Outline each blood parasite and name the species.
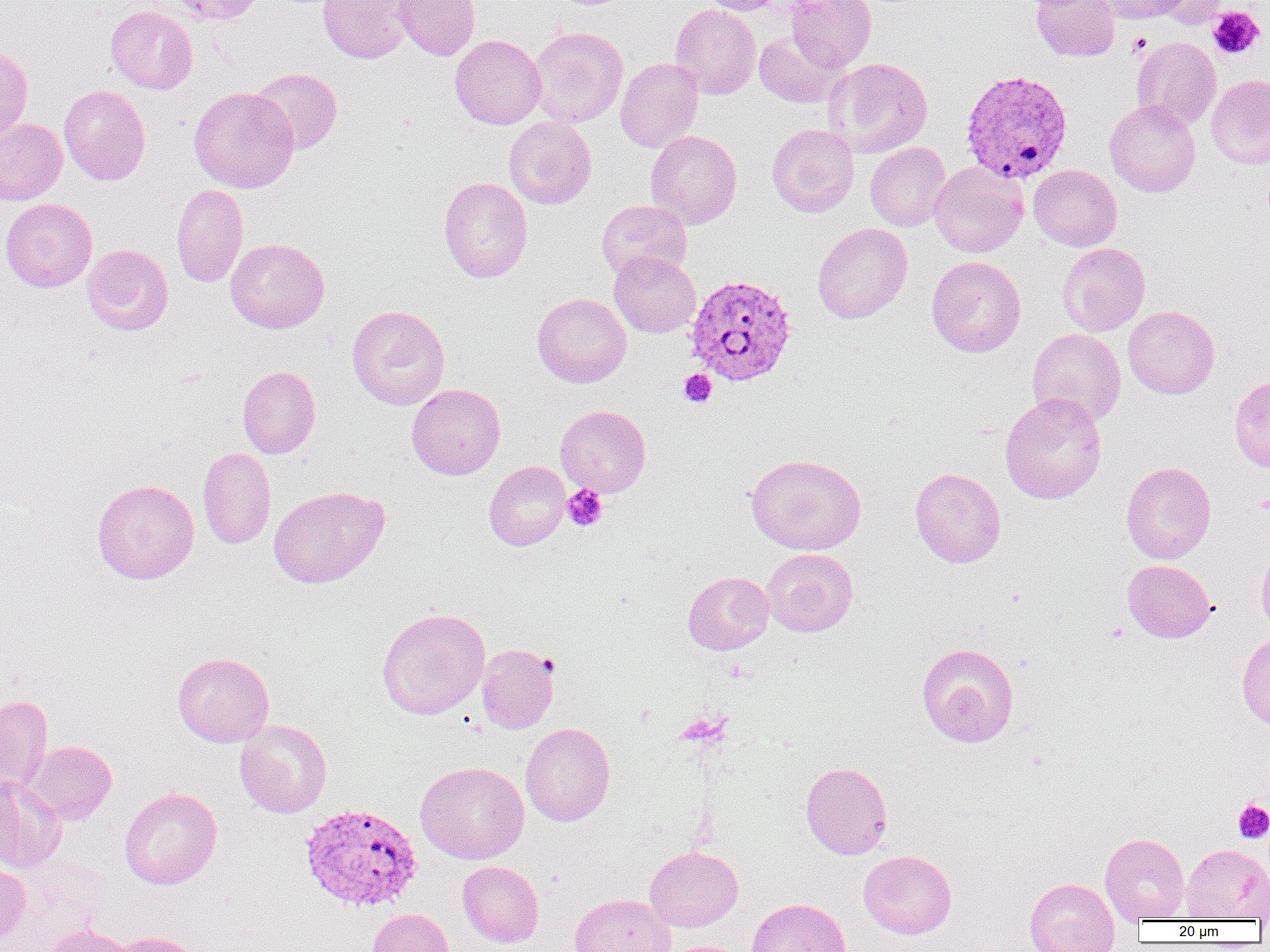

Approximate bounding boxes as named x1/y1/x2/y2 corners in pixels.
Plasmodium vivax-infected red blood cells: (x1=961, y1=69, x2=1073, y2=184), (x1=686, y1=274, x2=797, y2=386), (x1=300, y1=803, x2=423, y2=912).
No Plasmodium falciparum, Plasmodium ovale, Plasmodium malariae, Babesia divergens, or Trypanosoma brucei observed.

Uninfected red blood cell locations: (x1=164, y1=0, x2=266, y2=26), (x1=317, y1=0, x2=416, y2=63), (x1=394, y1=0, x2=480, y2=60), (x1=700, y1=0, x2=784, y2=14), (x1=786, y1=0, x2=876, y2=72), (x1=1032, y1=0, x2=1119, y2=61), (x1=1095, y1=0, x2=1190, y2=24), (x1=1154, y1=0, x2=1229, y2=29), (x1=670, y1=4, x2=761, y2=99), (x1=106, y1=6, x2=198, y2=94), (x1=528, y1=27, x2=628, y2=128), (x1=754, y1=32, x2=846, y2=107), (x1=450, y1=35, x2=546, y2=129), (x1=1131, y1=37, x2=1221, y2=130), (x1=0, y1=45, x2=33, y2=142), (x1=615, y1=57, x2=703, y2=152), (x1=823, y1=57, x2=933, y2=158), (x1=249, y1=67, x2=343, y2=155), (x1=1206, y1=74, x2=1270, y2=169), (x1=59, y1=85, x2=150, y2=185), (x1=189, y1=86, x2=299, y2=193), (x1=1105, y1=99, x2=1200, y2=197), (x1=0, y1=117, x2=67, y2=205), (x1=504, y1=117, x2=596, y2=208), (x1=767, y1=124, x2=859, y2=217), (x1=645, y1=130, x2=742, y2=228), (x1=865, y1=142, x2=951, y2=231), (x1=929, y1=161, x2=1028, y2=257), (x1=1028, y1=164, x2=1122, y2=251), (x1=439, y1=177, x2=532, y2=283), (x1=171, y1=183, x2=248, y2=288), (x1=0, y1=198, x2=97, y2=292), (x1=596, y1=200, x2=692, y2=282), (x1=813, y1=223, x2=912, y2=324), (x1=226, y1=238, x2=329, y2=333), (x1=1057, y1=243, x2=1150, y2=336), (x1=83, y1=244, x2=173, y2=335), (x1=609, y1=251, x2=700, y2=337), (x1=927, y1=256, x2=1025, y2=357), (x1=532, y1=293, x2=631, y2=388), (x1=347, y1=305, x2=450, y2=410), (x1=1123, y1=305, x2=1219, y2=398), (x1=1028, y1=328, x2=1126, y2=426), (x1=237, y1=365, x2=320, y2=458), (x1=1230, y1=375, x2=1270, y2=472), (x1=407, y1=384, x2=505, y2=480), (x1=1000, y1=392, x2=1107, y2=504), (x1=555, y1=405, x2=651, y2=497), (x1=198, y1=447, x2=276, y2=549), (x1=746, y1=453, x2=866, y2=554), (x1=484, y1=461, x2=570, y2=550), (x1=1121, y1=461, x2=1216, y2=564), (x1=910, y1=467, x2=1006, y2=568), (x1=92, y1=479, x2=199, y2=584), (x1=268, y1=485, x2=390, y2=588), (x1=1257, y1=540, x2=1270, y2=636), (x1=762, y1=548, x2=858, y2=636), (x1=1122, y1=559, x2=1216, y2=642), (x1=683, y1=571, x2=774, y2=654), (x1=377, y1=608, x2=490, y2=719), (x1=1237, y1=632, x2=1270, y2=731), (x1=916, y1=643, x2=1019, y2=747), (x1=476, y1=644, x2=558, y2=734), (x1=173, y1=652, x2=274, y2=747), (x1=0, y1=695, x2=53, y2=795), (x1=234, y1=719, x2=332, y2=818), (x1=521, y1=722, x2=615, y2=826), (x1=23, y1=741, x2=116, y2=824), (x1=416, y1=761, x2=529, y2=864), (x1=801, y1=762, x2=892, y2=859), (x1=0, y1=775, x2=66, y2=873), (x1=120, y1=787, x2=222, y2=889), (x1=1100, y1=832, x2=1190, y2=923), (x1=1181, y1=844, x2=1269, y2=920), (x1=644, y1=846, x2=743, y2=931), (x1=858, y1=849, x2=957, y2=939), (x1=0, y1=859, x2=31, y2=947), (x1=457, y1=861, x2=544, y2=948), (x1=1025, y1=877, x2=1120, y2=952), (x1=569, y1=893, x2=676, y2=952), (x1=747, y1=897, x2=850, y2=952), (x1=367, y1=908, x2=455, y2=952), (x1=43, y1=925, x2=135, y2=952), (x1=110, y1=932, x2=203, y2=952), (x1=662, y1=940, x2=754, y2=952). Platelet locations: (x1=1208, y1=6, x2=1264, y2=59), (x1=1128, y1=34, x2=1151, y2=56), (x1=679, y1=369, x2=717, y2=407), (x1=562, y1=485, x2=608, y2=531), (x1=1233, y1=799, x2=1270, y2=843). Slide-level diagnosis: Plasmodium vivax. 1000x magnification. One field of a larger specimen. Image is 1270×952 pixels. Thin blood film. Light microscopy.